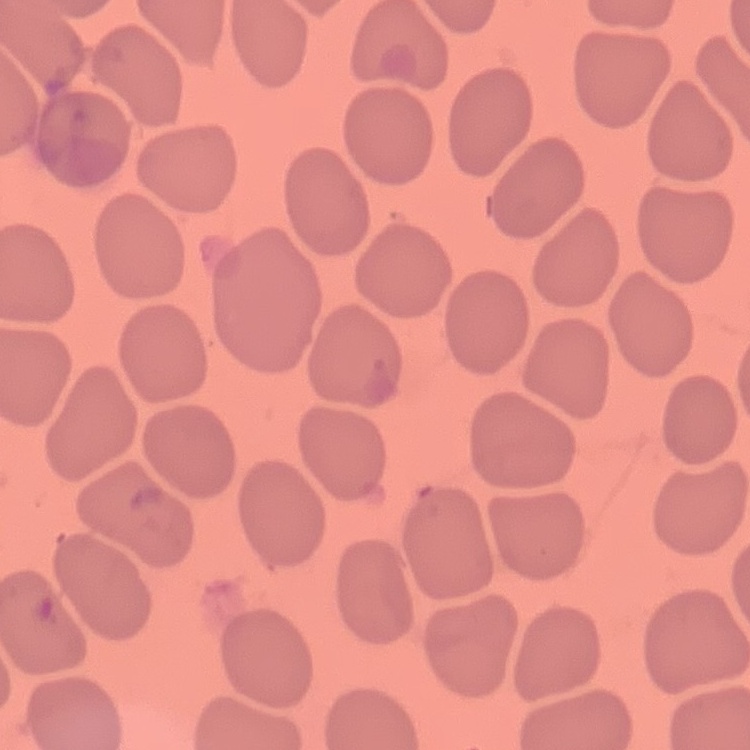
The red blood cells show no rouleaux formation. Field's or Giemsa stain. Square crop of a larger photomicrograph. Thin peripheral smear.